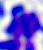
{
  "identification": "white blood cell",
  "modality": "photomicrograph",
  "magnification": "400x"
}